Locate and identify every blood parasite.
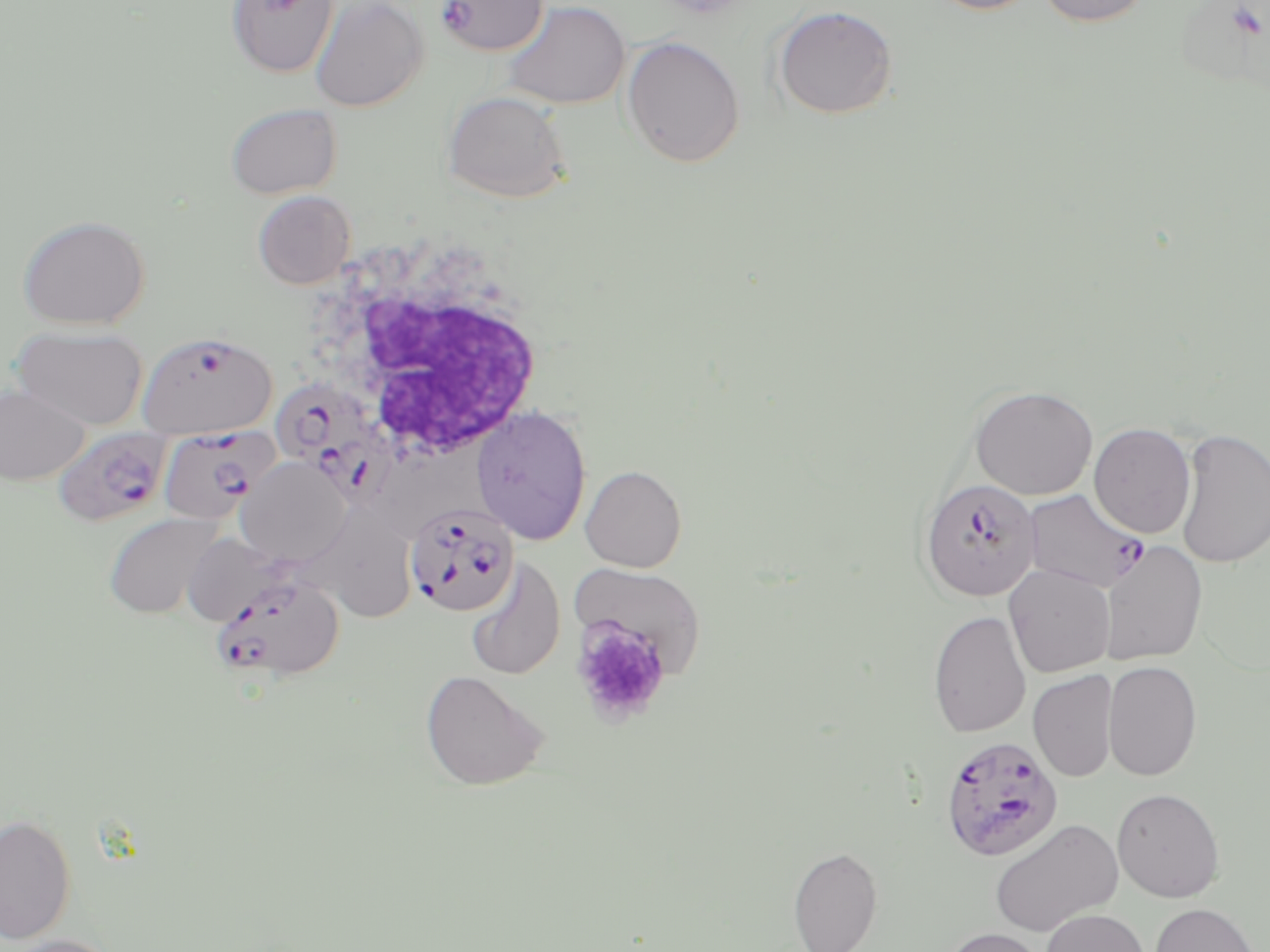
Approximate bounding boxes as (x1, y1, x2, y2) in pixels.
Plasmodium falciparum-infected red blood cells: (434, 0, 549, 57), (137, 330, 278, 438), (268, 378, 402, 503), (156, 426, 276, 525), (52, 427, 172, 527), (919, 477, 1041, 601), (1022, 489, 1149, 593), (404, 501, 519, 617), (208, 574, 344, 682), (939, 735, 1064, 862).
No Plasmodium ovale, Plasmodium malariae, Plasmodium vivax, Babesia divergens, or Trypanosoma brucei observed.

White blood cell locations: (304, 233, 552, 469). Platelet locations: (572, 618, 672, 725). Uninfected red blood cell locations: (226, 0, 339, 78), (308, 0, 428, 112), (924, 0, 1043, 15), (1034, 0, 1154, 27), (499, 1, 631, 110), (772, 4, 899, 120), (621, 35, 745, 168), (441, 90, 572, 203), (225, 103, 343, 199), (252, 190, 356, 290), (17, 215, 152, 330), (12, 324, 148, 431), (969, 384, 1098, 500), (0, 385, 90, 485), (471, 405, 591, 545), (1089, 423, 1196, 539), (1174, 427, 1270, 569), (236, 456, 352, 568), (580, 465, 686, 572), (103, 512, 224, 620), (283, 512, 426, 630), (180, 532, 294, 627), (1100, 539, 1208, 666), (465, 558, 566, 681), (570, 562, 706, 678), (1004, 565, 1115, 678), (928, 610, 1031, 738), (1103, 660, 1203, 781), (420, 670, 549, 790), (1028, 670, 1118, 782), (1112, 788, 1226, 902), (0, 813, 77, 945), (988, 818, 1123, 937), (788, 845, 884, 952), (1148, 902, 1261, 952), (1040, 908, 1149, 952), (939, 927, 1052, 952), (1, 934, 123, 952). Slide-level diagnosis: Plasmodium falciparum. Captured at 1000x magnification. Optical microscopy. Image is 1270×952 pixels. May-Grünwald-Giemsa-stained preparation. Thin blood film. One field of a larger specimen.